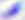

Summary:
  - Modality: photomicrograph
  - Magnification: 400x
  - Identification: Toxoplasma gondii